Classify this cell by malaria status.
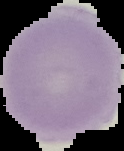
Uninfected.

Summary:
  - Image size: 124×151 pixels
  - Image type: segmented cell region with the area outside set to black
  - Preparation: thin blood smear